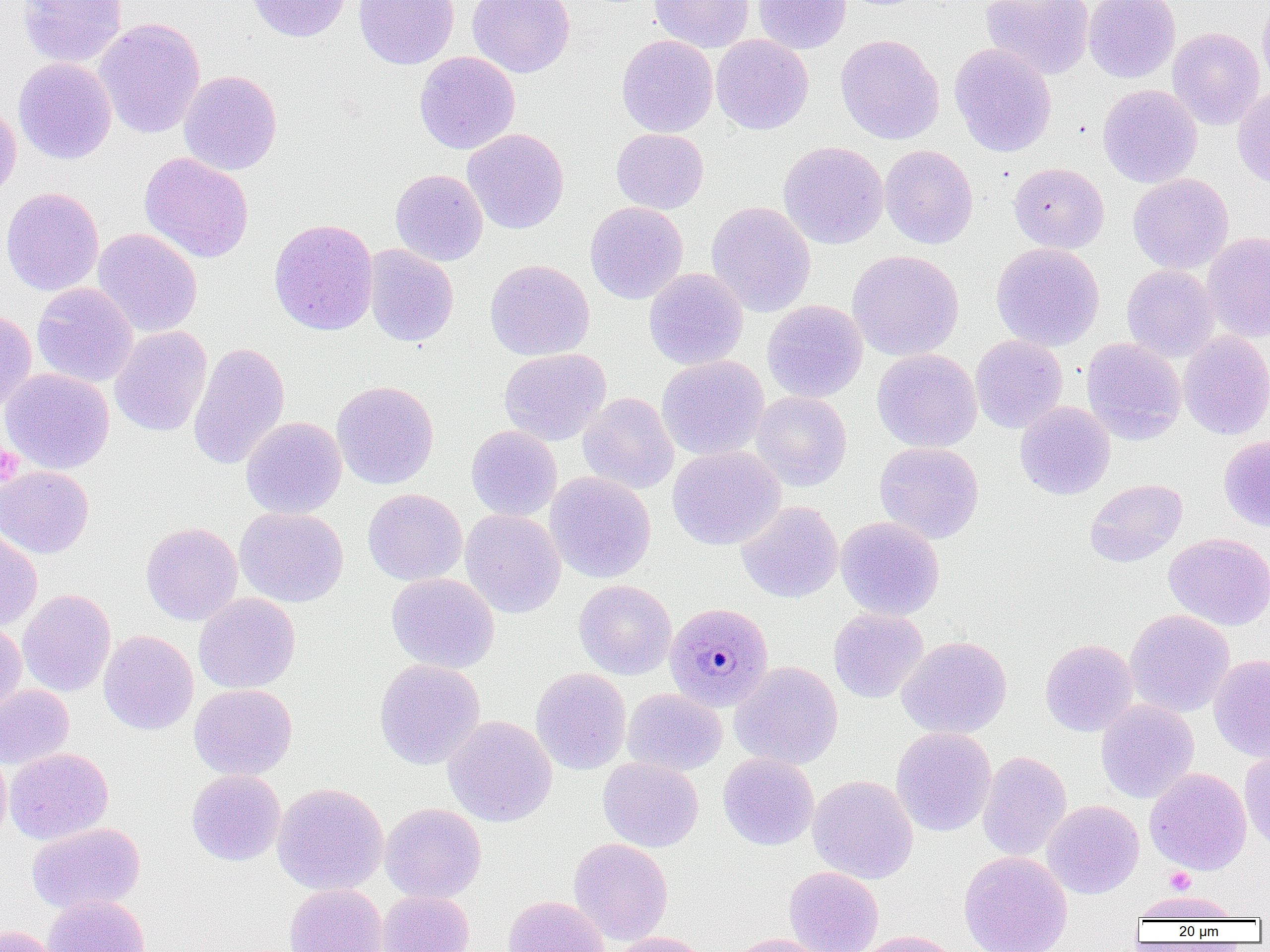

slide-level diagnosis = Plasmodium malariae
preparation = thin blood smear
Plasmodium malariae-infected red blood cell locations = approximate bounding boxes as (x1,y1)-(x2,y2) corner pairs in pixels: (664,602)-(773,711)
modality = light microscopy
uninfected red blood cell locations = approximate bounding boxes as (x1,y1)-(x2,y2) corner pairs in pixels: (17,0)-(127,68), (245,0)-(352,42), (354,0)-(459,69), (467,0)-(575,78), (649,0)-(755,53), (753,0)-(851,54), (980,0)-(1095,80), (1083,0)-(1181,83), (1257,0)-(1270,96), (94,18)-(205,139), (1167,28)-(1265,130), (616,34)-(718,137), (835,34)-(944,145), (711,35)-(814,135), (949,43)-(1057,156), (414,51)-(520,154), (13,58)-(116,164), (178,70)-(282,175), (1098,84)-(1202,188), (1233,85)-(1270,189), (0,101)-(21,204), (462,128)-(569,234), (611,128)-(709,214), (778,141)-(889,249), (879,145)-(978,249), (139,152)-(254,263), (1008,162)-(1109,253), (390,169)-(488,266), (1128,173)-(1234,274), (1,186)-(105,296), (585,201)-(688,304), (706,201)-(816,317), (269,218)-(378,336), (92,228)-(202,338), (1202,232)-(1270,343), (991,242)-(1105,351), (364,244)-(458,347), (847,250)-(964,361), (484,259)-(595,361), (1122,264)-(1220,361), (644,268)-(748,370), (31,282)-(138,387), (761,299)-(868,403), (0,310)-(37,412), (109,326)-(212,437), (1179,330)-(1270,440), (970,335)-(1068,433), (1082,337)-(1186,444), (188,342)-(290,470), (499,348)-(611,445), (871,349)-(982,452), (657,355)-(769,461), (0,368)-(115,474), (331,380)-(439,489), (750,391)-(852,491), (578,392)-(679,494), (1015,401)-(1115,500), (240,417)-(346,519), (466,425)-(562,521), (1218,436)-(1270,531), (874,442)-(984,543), (667,446)-(785,550), (0,466)-(94,559), (545,471)-(656,583), (1085,479)-(1187,567), (363,488)-(467,586), (737,501)-(843,602), (234,507)-(348,607), (459,509)-(565,617), (835,516)-(944,620), (140,521)-(243,625), (0,527)-(42,631), (1163,533)-(1270,631), (386,573)-(500,673), (575,580)-(677,680), (18,589)-(116,697), (193,592)-(300,694), (828,608)-(928,703), (1124,609)-(1235,717), (0,621)-(27,716), (98,630)-(199,735), (896,635)-(1012,739), (1040,639)-(1138,737), (1209,654)-(1270,762), (374,659)-(485,770), (729,661)-(842,769), (531,667)-(632,774), (0,684)-(74,768), (188,684)-(297,780), (622,689)-(727,775), (1096,699)-(1199,803), (443,715)-(557,827), (891,726)-(996,837), (0,746)-(11,845), (1240,747)-(1270,853), (4,748)-(113,845), (977,750)-(1072,861), (718,753)-(819,850), (598,756)-(703,852), (1145,767)-(1251,875), (186,770)-(285,866), (808,775)-(918,884), (272,782)-(388,895), (1042,800)-(1144,899), (380,803)-(486,903), (26,822)-(145,914), (568,837)-(673,945), (958,850)-(1073,952), (784,866)-(883,951), (284,883)-(388,952), (377,890)-(475,952), (1130,890)-(1244,922), (42,894)-(150,952), (503,895)-(610,952), (0,924)-(61,952), (849,931)-(962,952), (607,932)-(714,952), (721,933)-(833,952)
platelet locations = approximate bounding boxes as (x1,y1)-(x2,y2) corner pairs in pixels: (0,444)-(23,485), (1166,867)-(1196,895)
image size = 1270×952 pixels
magnification = 1000x
field of view = single